Mark where platelets are.
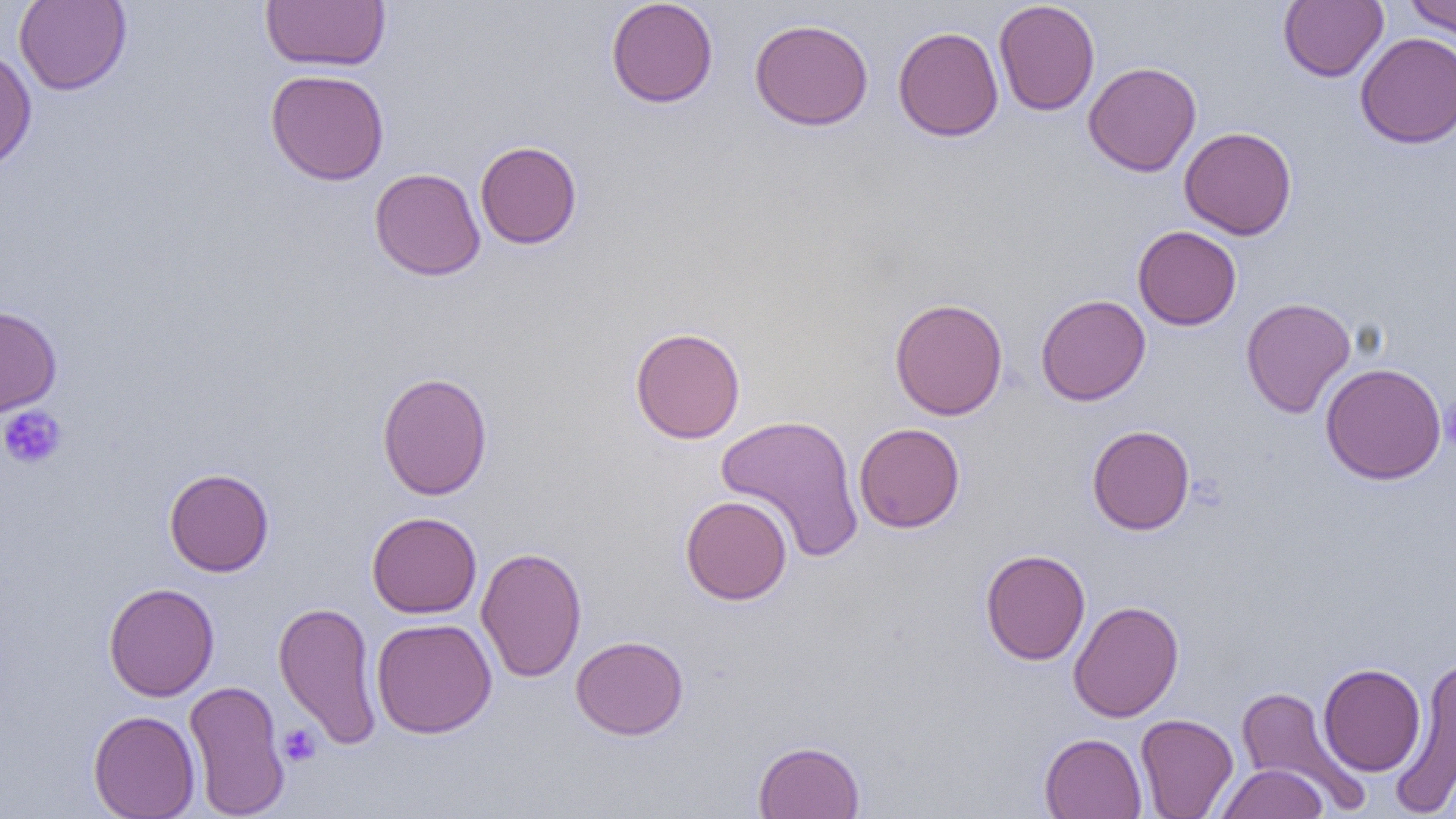
Approximate bounding boxes as [x1, y1, x2, y2] in pixels.
Platelets: [1439, 397, 1456, 453], [0, 405, 67, 470], [279, 723, 321, 767].

{
  "slide_level_diagnosis": "negative for blood parasites",
  "magnification": "1000x",
  "image_size": "1456×819 pixels",
  "modality": "light microscopy",
  "preparation": "thin blood smear",
  "uninfected_red_blood_cell_locations": "approximate bounding boxes as [x1, y1, x2, y2] in pixels: [14, 0, 131, 95], [260, 0, 391, 71], [606, 0, 719, 108], [993, 0, 1100, 116], [1403, 0, 1456, 37], [1279, 1, 1388, 82], [749, 18, 874, 131], [892, 26, 1004, 142], [1355, 32, 1456, 149], [0, 47, 37, 174], [1083, 61, 1201, 177], [265, 68, 390, 185], [1179, 126, 1297, 240], [475, 140, 582, 249], [369, 168, 485, 281], [1132, 225, 1241, 330], [1035, 294, 1151, 405], [1241, 296, 1356, 418], [889, 297, 1008, 420], [0, 305, 62, 417], [629, 327, 746, 444], [1320, 363, 1447, 485], [377, 371, 492, 501], [715, 414, 865, 562], [853, 422, 965, 533], [1086, 425, 1195, 535], [164, 467, 274, 577], [680, 495, 793, 605], [367, 511, 483, 618], [475, 546, 587, 683], [980, 548, 1091, 665], [103, 582, 219, 701], [273, 600, 383, 750], [1068, 600, 1184, 722], [371, 617, 497, 738], [569, 635, 689, 740], [1390, 655, 1456, 818], [1318, 663, 1426, 776], [183, 679, 290, 818], [1234, 685, 1367, 811], [88, 710, 200, 819], [1135, 714, 1238, 819], [1039, 732, 1147, 819], [753, 740, 865, 818], [1216, 763, 1328, 819]",
  "field_of_view": "one of a larger specimen"
}